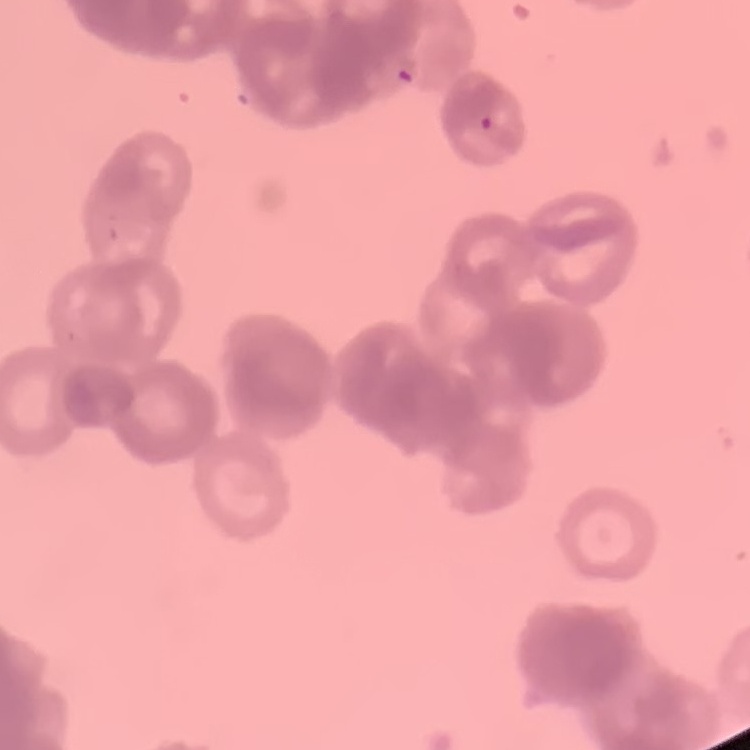
The red blood cells exhibit rouleaux formation. Stained with either Field's or Giemsa. Thin blood film. One tile cut from a larger photomicrograph.